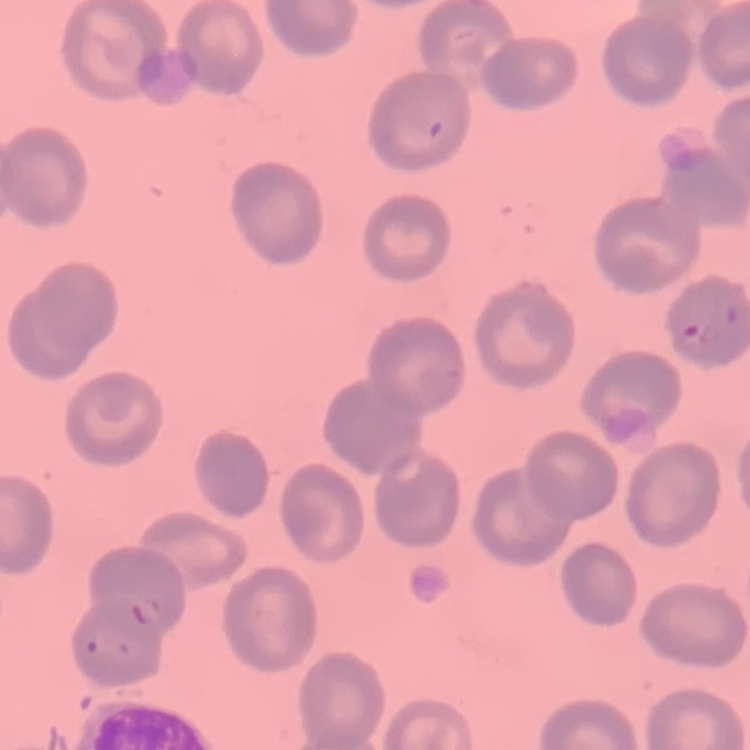

red blood cell morphology = no rouleaux formation
stain = Field's or Giemsa
preparation = thin peripheral smear
image type = square crop of a larger photomicrograph